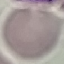

Malaria status: uninfected. Giemsa stain. Thin blood smear. Automatically extracted cell patch, resized to 64 × 64 pixels. Acquired by smartphone through the microscope eyepiece.